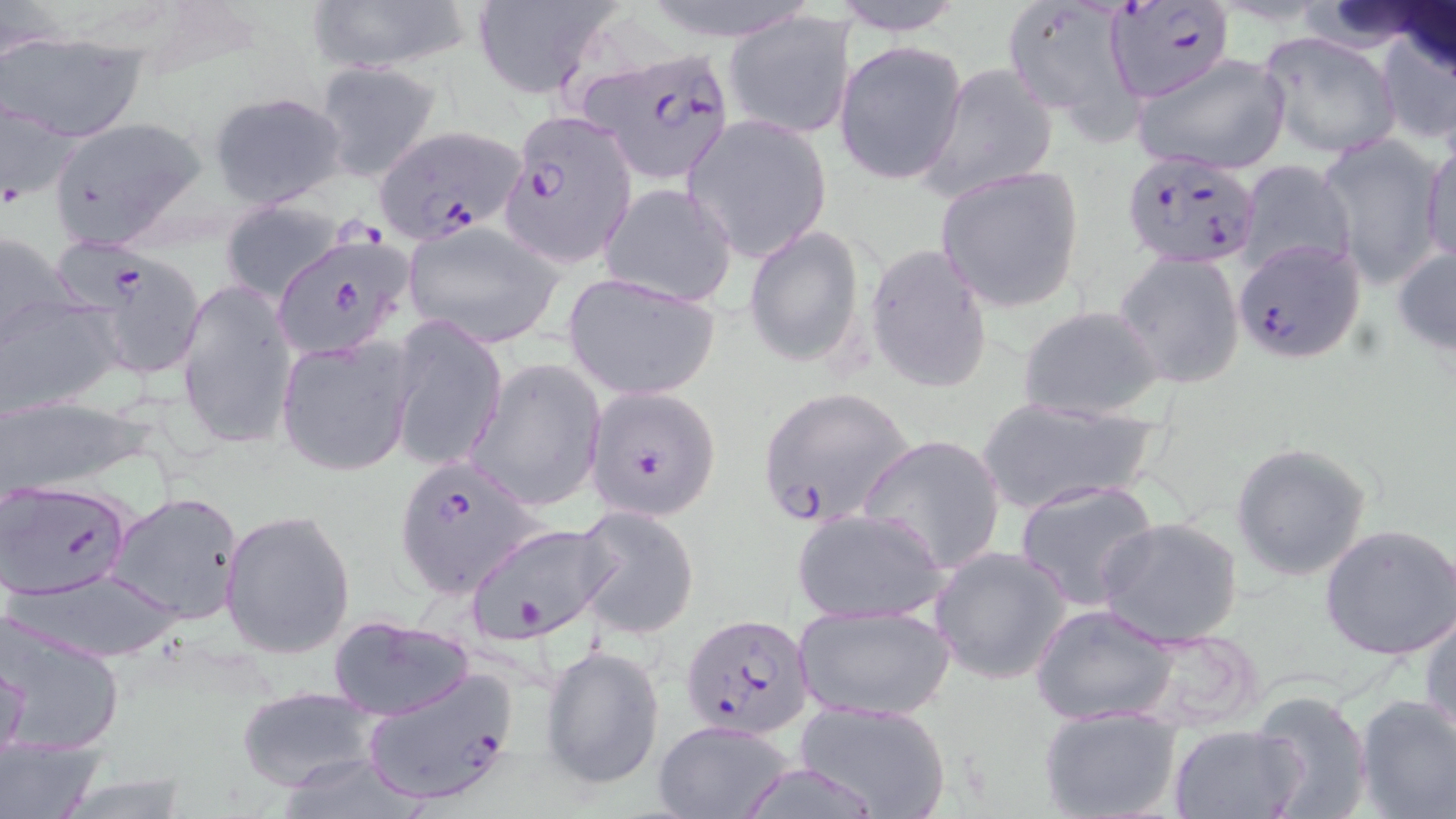

slide-level diagnosis = Plasmodium falciparum
preparation = thin blood smear
Plasmodium falciparum-infected red blood cell locations = approximate bounding boxes as (x1,y1)-(x2,y2) corner pairs in pixels: (1105,0)-(1232,101), (583,48)-(736,186), (503,107)-(639,266), (371,123)-(527,248), (1120,149)-(1261,270), (274,233)-(417,359), (1232,237)-(1367,362), (86,252)-(207,381), (583,385)-(722,522), (756,386)-(916,530), (392,455)-(540,599), (1,478)-(132,599), (682,613)-(813,739), (359,668)-(518,807)
modality = optical microscopy
uninfected red blood cell locations = approximate bounding boxes as (x1,y1)-(x2,y2) corner pairs in pixels: (305,0)-(472,75), (823,0)-(971,35), (1002,0)-(1149,136), (468,1)-(622,99), (725,9)-(857,140), (1372,20)-(1456,149), (1258,30)-(1401,161), (2,31)-(146,142), (834,39)-(968,185), (1129,52)-(1292,176), (313,60)-(443,183), (917,64)-(1059,200), (207,89)-(350,209), (1,95)-(82,211), (684,114)-(832,262), (47,116)-(210,250), (1421,134)-(1456,273), (1318,135)-(1449,289), (1236,160)-(1357,278), (935,165)-(1085,313), (598,182)-(738,308), (220,198)-(344,303), (404,224)-(562,346), (744,224)-(866,368), (0,228)-(81,358), (1392,239)-(1456,358), (865,243)-(993,393), (1115,252)-(1245,389), (563,273)-(722,401), (177,278)-(296,454), (0,294)-(126,418), (1017,304)-(1166,422), (388,317)-(506,476), (276,335)-(416,477), (466,358)-(606,510), (0,395)-(149,497), (972,396)-(1160,517), (859,432)-(1009,575), (1231,442)-(1373,581), (1014,479)-(1162,612), (108,492)-(243,624), (573,506)-(700,639), (792,507)-(950,624), (216,508)-(350,658), (1098,516)-(1244,647), (465,521)-(613,645), (1321,523)-(1456,660), (928,544)-(1073,685), (8,567)-(187,664), (793,602)-(956,720), (1031,604)-(1179,726), (1419,607)-(1456,741), (1,611)-(127,758), (328,615)-(476,722), (1130,629)-(1269,733), (540,642)-(665,791), (1,651)-(28,768), (237,687)-(380,791), (1248,689)-(1374,819), (1353,694)-(1456,819), (793,700)-(952,818), (1038,708)-(1183,819), (650,718)-(800,819), (1169,725)-(1305,818), (0,733)-(106,819)
magnification = 1000x
field of view = one of a larger specimen
stain = May-Grünwald-Giemsa
image size = 1456×819 pixels